State which parasite is depicted.
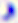
This is Toxoplasma gondii.

modality = photomicrograph
magnification = 400x